Locate and identify every blood parasite.
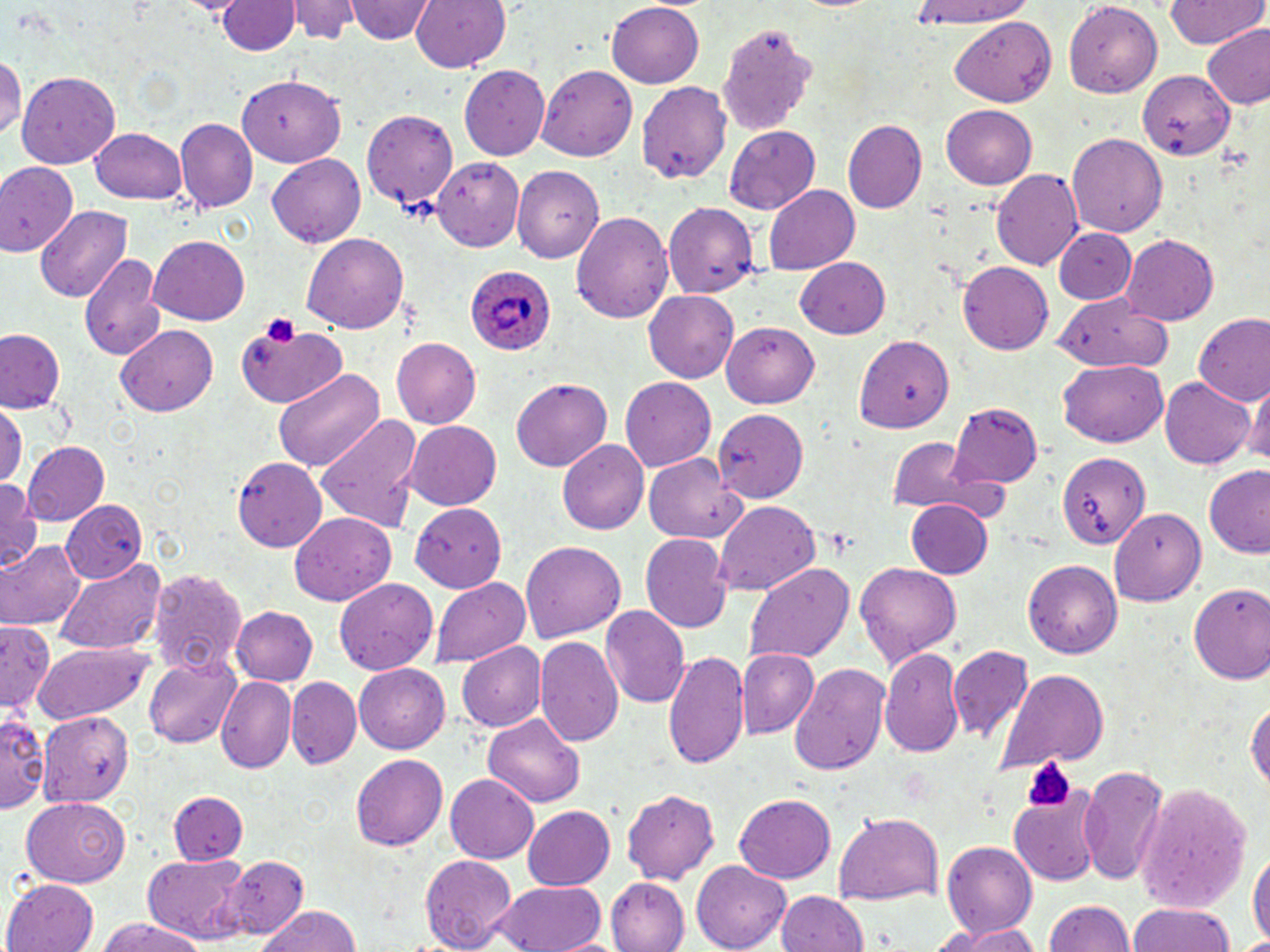
Approximate bounding boxes as [x1, y1, x2, y2] in pixels.
Plasmodium ovale-infected red blood cells: [466, 265, 558, 356].
No Plasmodium falciparum, Plasmodium malariae, Plasmodium vivax, Babesia divergens, or Trypanosoma brucei observed.

Summary:
  - Platelet locations: [262, 313, 302, 347], [1029, 760, 1074, 809]
  - Uninfected red blood cell locations: [291, 0, 356, 43], [346, 0, 433, 45], [409, 0, 511, 73], [1065, 1, 1163, 95], [1162, 1, 1268, 49], [219, 2, 298, 54], [607, 2, 705, 89], [904, 2, 1036, 30], [951, 17, 1058, 108], [718, 26, 812, 136], [1202, 26, 1270, 111], [0, 54, 25, 142], [537, 63, 640, 160], [458, 65, 550, 160], [1137, 68, 1233, 160], [16, 72, 121, 169], [239, 75, 347, 167], [639, 80, 736, 184], [941, 105, 1038, 191], [362, 109, 459, 207], [174, 118, 257, 214], [845, 118, 931, 214], [724, 126, 820, 212], [88, 127, 186, 204], [1068, 133, 1168, 240], [267, 154, 369, 247], [431, 157, 527, 246], [0, 162, 77, 256], [515, 165, 608, 262], [993, 168, 1083, 273], [2, 172, 121, 282], [765, 185, 859, 274], [664, 201, 757, 297], [37, 205, 134, 302], [571, 209, 673, 323], [1052, 226, 1135, 304], [303, 233, 407, 336], [1119, 234, 1216, 326], [149, 236, 249, 324], [79, 251, 164, 361], [795, 257, 892, 338], [959, 261, 1054, 354], [644, 291, 738, 384], [1058, 302, 1169, 373], [1193, 314, 1270, 403], [237, 320, 347, 410], [721, 322, 817, 408], [117, 323, 218, 416], [0, 328, 64, 414], [855, 335, 952, 431], [391, 338, 481, 427], [1057, 360, 1168, 447], [271, 367, 384, 474], [1160, 377, 1255, 469], [513, 378, 611, 471], [622, 378, 716, 472], [1247, 379, 1268, 472], [948, 402, 1045, 485], [0, 406, 24, 489], [713, 409, 807, 503], [316, 414, 422, 534], [404, 421, 500, 511], [883, 435, 987, 518], [558, 440, 653, 533], [24, 442, 110, 528], [646, 452, 746, 542], [1058, 452, 1149, 552], [233, 456, 325, 551], [1201, 468, 1270, 558], [0, 481, 44, 571], [904, 499, 994, 580], [62, 500, 149, 584], [714, 502, 821, 596], [410, 504, 505, 590], [1105, 510, 1205, 608], [288, 512, 395, 607], [642, 533, 733, 635], [1, 540, 82, 630], [520, 541, 627, 645], [53, 556, 167, 656], [1022, 558, 1120, 659], [855, 562, 963, 670], [745, 563, 852, 669], [148, 567, 247, 677], [333, 576, 436, 674], [429, 577, 528, 669], [1185, 582, 1270, 683], [231, 606, 318, 688], [599, 607, 688, 710], [0, 626, 56, 718], [535, 637, 624, 751], [30, 642, 161, 725], [455, 642, 548, 732], [947, 646, 1035, 744], [663, 647, 752, 773], [880, 648, 965, 757], [738, 649, 817, 737], [146, 657, 242, 746], [787, 662, 892, 777], [355, 665, 451, 753], [997, 669, 1108, 770], [218, 678, 297, 772], [286, 679, 361, 768], [1245, 695, 1270, 793], [0, 709, 46, 816], [39, 710, 135, 806], [482, 712, 586, 809], [352, 755, 447, 850], [1078, 764, 1168, 885], [443, 772, 538, 864], [1010, 784, 1104, 887], [1138, 786, 1252, 911], [622, 789, 720, 885], [173, 791, 249, 866], [735, 791, 836, 882], [22, 797, 130, 886], [520, 805, 616, 890], [834, 811, 945, 905], [943, 842, 1036, 937], [1247, 846, 1268, 952], [419, 852, 516, 952], [141, 854, 250, 944], [228, 856, 308, 937], [691, 861, 789, 950], [605, 874, 689, 950], [6, 877, 100, 952], [494, 879, 608, 952], [773, 891, 869, 952], [1041, 899, 1137, 951], [1130, 901, 1237, 952], [255, 906, 362, 952], [91, 919, 210, 952], [945, 924, 1043, 951]
  - Slide-level diagnosis: Plasmodium ovale
  - Modality: optical microscopy
  - Image size: 1270×952 pixels
  - Preparation: thin blood film
  - Magnification: 1000x
  - Stain: May-Grünwald-Giemsa
  - Field of view: one of a larger specimen